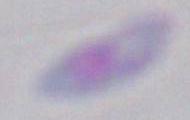
Summary:
  - Identification: Toxoplasma gondii
  - Modality: micrograph
  - Magnification: 1000x